Locate every parasitized RBC.
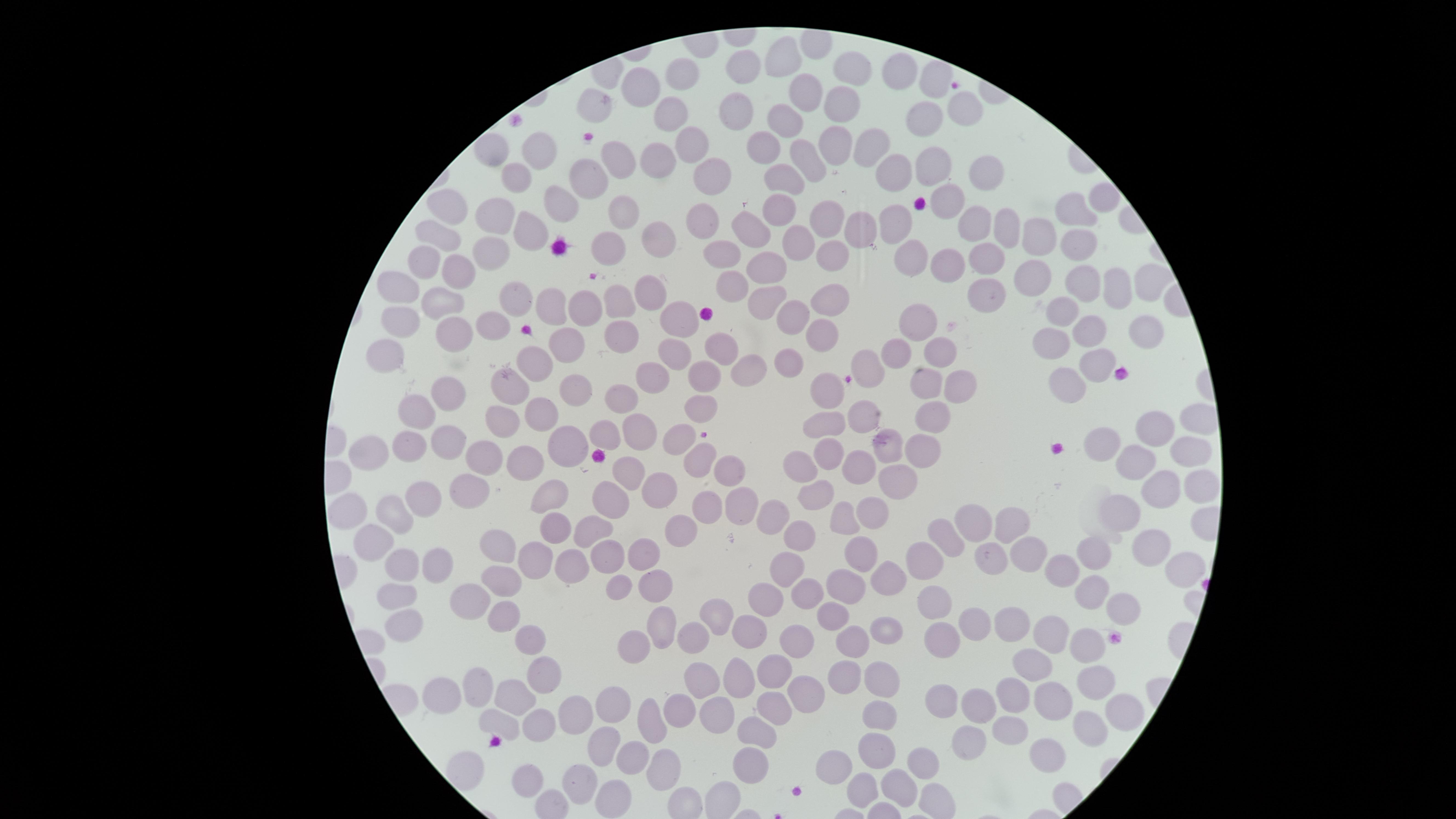
No parasitized RBCs identified.

image_size: 1456×819 pixels
preparation: thin smear of blood
uninfected_RBCs: 'approximate marker points, in pixels from the top-left corner: (x=787, y=56), (x=852, y=65), (x=741, y=67), (x=903, y=71), (x=677, y=77), (x=939, y=78), (x=649, y=83), (x=801, y=98), (x=834, y=102), (x=598, y=104), (x=960, y=108), (x=736, y=112), (x=789, y=112), (x=673, y=113), (x=925, y=116), (x=833, y=139), (x=768, y=140), (x=692, y=147), (x=493, y=150), (x=860, y=151), (x=539, y=153), (x=621, y=156), (x=806, y=156), (x=936, y=159), (x=662, y=163), (x=980, y=168), (x=791, y=170), (x=711, y=173), (x=903, y=173), (x=515, y=174), (x=592, y=175), (x=1104, y=198), (x=560, y=201), (x=947, y=202), (x=781, y=203), (x=453, y=207), (x=1077, y=210), (x=622, y=211), (x=487, y=219), (x=828, y=219), (x=701, y=221), (x=897, y=221), (x=975, y=225), (x=752, y=227), (x=1004, y=228), (x=862, y=231), (x=440, y=233), (x=525, y=235), (x=1036, y=235), (x=801, y=236), (x=658, y=237), (x=609, y=240), (x=1079, y=247), (x=729, y=250), (x=491, y=252), (x=832, y=257), (x=427, y=260), (x=913, y=260), (x=989, y=261), (x=770, y=264), (x=954, y=264), (x=456, y=275), (x=1036, y=279), (x=737, y=281), (x=1147, y=281), (x=1084, y=282), (x=395, y=286), (x=655, y=289), (x=988, y=289), (x=1117, y=289), (x=515, y=298), (x=828, y=299), (x=768, y=301), (x=444, y=304), (x=551, y=306), (x=584, y=306), (x=618, y=306), (x=1064, y=311), (x=792, y=314), (x=676, y=318), (x=921, y=320), (x=401, y=323), (x=1086, y=328), (x=491, y=329), (x=822, y=335), (x=1145, y=335), (x=452, y=337), (x=622, y=338), (x=1051, y=339), (x=566, y=343), (x=939, y=343), (x=672, y=348), (x=724, y=348), (x=902, y=352), (x=381, y=355), (x=789, y=360), (x=1097, y=360), (x=535, y=364), (x=868, y=366), (x=756, y=367), (x=706, y=374), (x=657, y=380), (x=926, y=381), (x=960, y=383), (x=1068, y=384), (x=514, y=385), (x=448, y=391), (x=830, y=391), (x=577, y=395), (x=627, y=401), (x=704, y=402), (x=418, y=410), (x=542, y=412), (x=930, y=412), (x=870, y=416), (x=502, y=418), (x=830, y=426), (x=640, y=428), (x=1149, y=428), (x=605, y=433), (x=685, y=435), (x=1109, y=441), (x=451, y=442), (x=886, y=446), (x=572, y=448), (x=918, y=448), (x=1188, y=449), (x=403, y=452), (x=368, y=454), (x=831, y=454), (x=485, y=456), (x=701, y=458), (x=524, y=459), (x=1133, y=459), (x=798, y=461), (x=865, y=465), (x=630, y=468), (x=729, y=468), (x=895, y=481), (x=1159, y=485), (x=1197, y=490), (x=663, y=491), (x=469, y=493), (x=820, y=495), (x=553, y=497), (x=613, y=501), (x=425, y=502), (x=711, y=506), (x=739, y=509), (x=360, y=511), (x=1125, y=512), (x=400, y=514), (x=871, y=514), (x=776, y=516), (x=844, y=518), (x=1011, y=521), (x=589, y=524), (x=550, y=526), (x=680, y=528), (x=976, y=530), (x=801, y=531), (x=941, y=539), (x=373, y=547), (x=1150, y=547), (x=502, y=551), (x=1100, y=552), (x=602, y=553), (x=649, y=555), (x=860, y=555), (x=989, y=556), (x=1025, y=558), (x=919, y=560), (x=539, y=561), (x=568, y=565), (x=1066, y=565), (x=789, y=567), (x=1180, y=567), (x=397, y=568), (x=433, y=568), (x=503, y=578), (x=887, y=580), (x=619, y=581), (x=847, y=585), (x=652, y=587), (x=803, y=589), (x=1091, y=590), (x=767, y=592), (x=471, y=595), (x=397, y=598), (x=940, y=610), (x=1121, y=610), (x=503, y=613), (x=1011, y=615), (x=713, y=616), (x=831, y=616), (x=402, y=618), (x=661, y=622), (x=751, y=624), (x=886, y=627), (x=1051, y=629), (x=974, y=631), (x=523, y=636), (x=687, y=638), (x=801, y=639), (x=943, y=641), (x=1089, y=643), (x=848, y=644), (x=633, y=652), (x=1032, y=667), (x=777, y=669), (x=742, y=670), (x=845, y=675), (x=541, y=678), (x=699, y=679), (x=876, y=679), (x=1096, y=679), (x=478, y=684), (x=439, y=686), (x=804, y=690), (x=1056, y=696), (x=517, y=697), (x=943, y=697), (x=1014, y=697), (x=775, y=705), (x=610, y=706), (x=985, y=706), (x=721, y=710), (x=677, y=711), (x=880, y=715), (x=1122, y=716), (x=568, y=720), (x=498, y=722), (x=653, y=724), (x=534, y=726), (x=1010, y=728), (x=1089, y=729), (x=756, y=731), (x=968, y=734), (x=606, y=741), (x=874, y=751), (x=1047, y=751), (x=634, y=757), (x=838, y=762), (x=749, y=763), (x=923, y=764), (x=662, y=766), (x=527, y=777), (x=580, y=783), (x=899, y=785), (x=863, y=789), (x=612, y=795)'
stain: Giemsa
field_of_view: single
capture: smartphone photograph through the microscope eyepiece
visible_region: circular